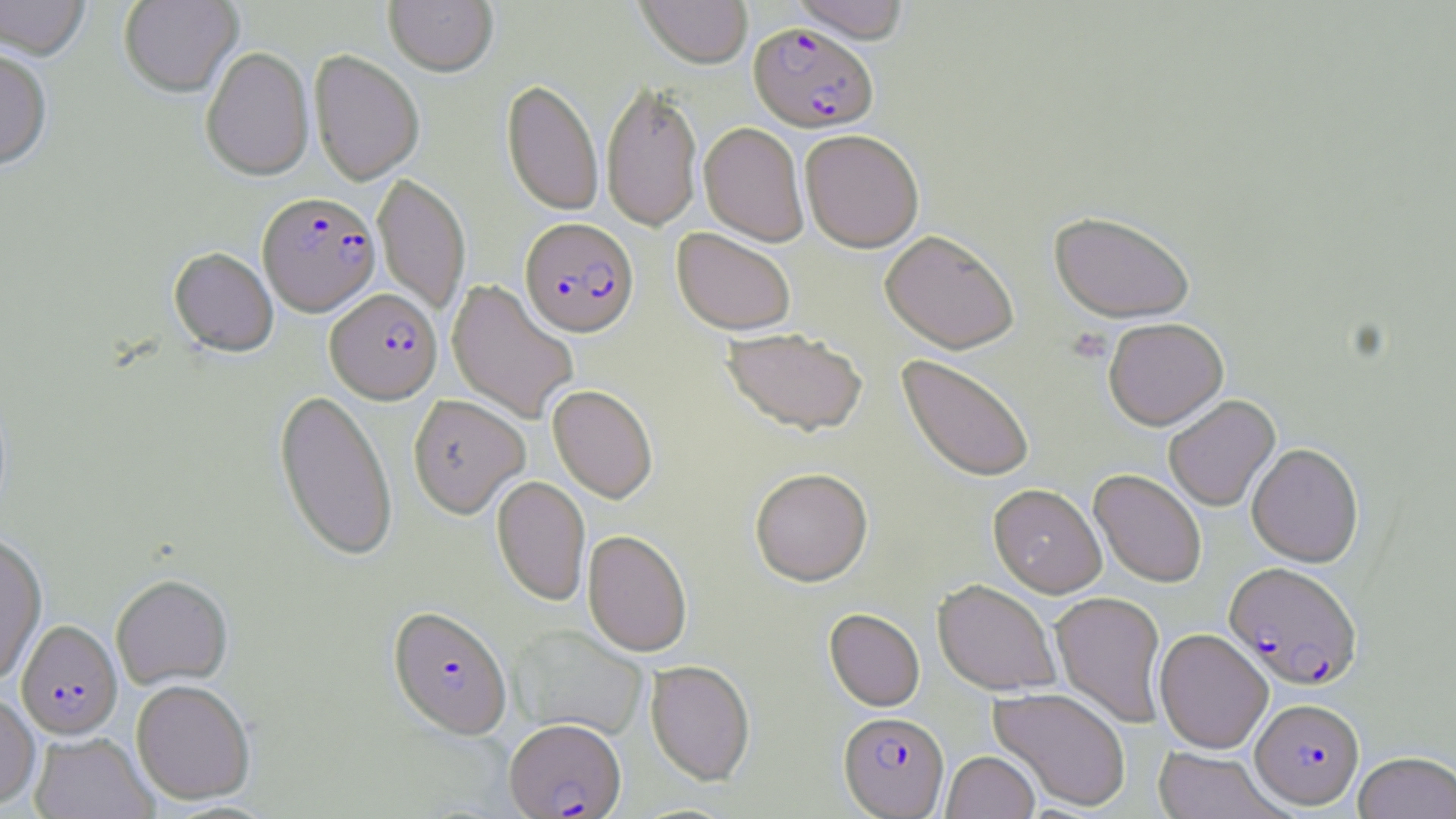
Summary:
  - Coordinate format: approximate bounding boxes as [x1, y1, x2, y2] in pixels
  - Platelet locations: [1066, 328, 1113, 364]
  - Plasmodium falciparum-infected red blood cell locations: [749, 22, 878, 133], [257, 192, 380, 316], [520, 218, 639, 338], [326, 289, 442, 404], [1224, 561, 1363, 690], [387, 606, 512, 740], [17, 620, 122, 739], [1251, 698, 1364, 808], [838, 711, 949, 817], [504, 719, 626, 819]
  - Uninfected red blood cell locations: [0, 0, 91, 61], [119, 0, 243, 98], [384, 0, 498, 76], [635, 0, 754, 68], [790, 0, 912, 42], [201, 46, 314, 182], [0, 48, 52, 172], [309, 50, 424, 185], [501, 79, 604, 216], [601, 80, 703, 232], [602, 100, 807, 237], [699, 122, 809, 246], [800, 130, 924, 252], [373, 173, 470, 315], [1049, 211, 1195, 323], [673, 227, 796, 335], [880, 229, 1019, 353], [168, 247, 278, 358], [446, 278, 579, 424], [1103, 317, 1228, 430], [722, 327, 869, 436], [898, 354, 1036, 483], [547, 385, 658, 503], [274, 389, 398, 563], [275, 392, 531, 538], [408, 394, 530, 517], [1164, 394, 1280, 512], [1247, 442, 1364, 567], [749, 467, 873, 586], [1089, 469, 1207, 588], [491, 475, 590, 606], [989, 484, 1106, 597], [582, 530, 692, 658], [0, 534, 47, 684], [111, 574, 233, 689], [932, 579, 1061, 696], [1050, 591, 1167, 728], [824, 609, 925, 711], [510, 624, 647, 739], [1154, 628, 1273, 753], [645, 660, 755, 785], [131, 679, 255, 805], [989, 686, 1131, 811], [0, 692, 40, 809], [29, 732, 157, 819], [1151, 746, 1289, 819], [941, 750, 1040, 819], [1353, 751, 1456, 819]
  - Slide-level diagnosis: Plasmodium falciparum
  - Magnification: 1000x
  - Field of view: one of a larger specimen
  - Modality: optical microscopy
  - Preparation: thin blood smear
  - Stain: May-Grünwald-Giemsa
  - Image size: 1456×819 pixels